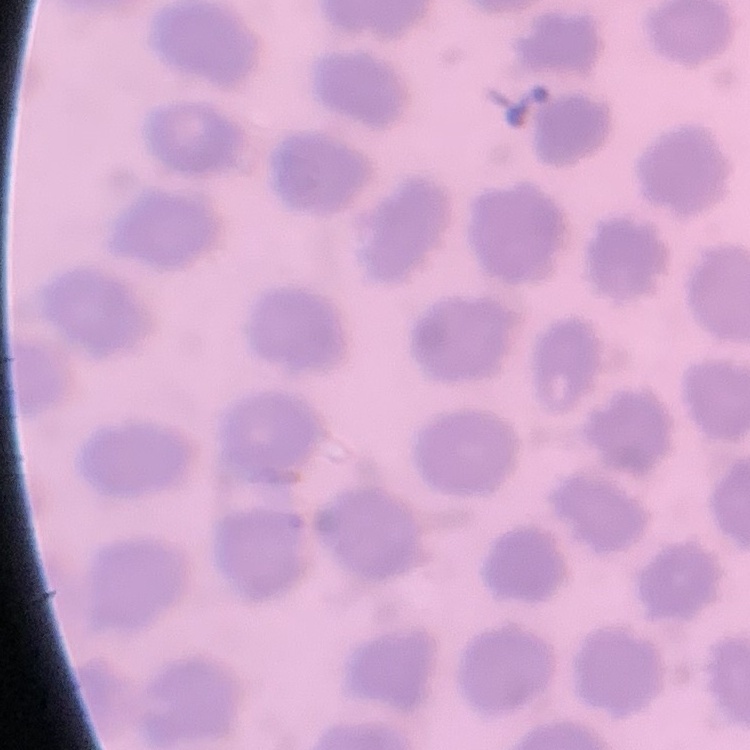

Summary:
  - Erythrocyte morphology: no rouleaux formation
  - Preparation: thin blood smear
  - Stain: Field's or Giemsa
  - Image type: square crop of a larger photomicrograph